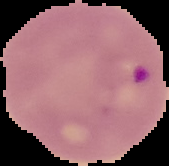
Result: Plasmodium parasites identified. The area outside the segmented cell region is set to black. From a thin blood smear. Image is 169×166 pixels.